Name the blood parasite species.
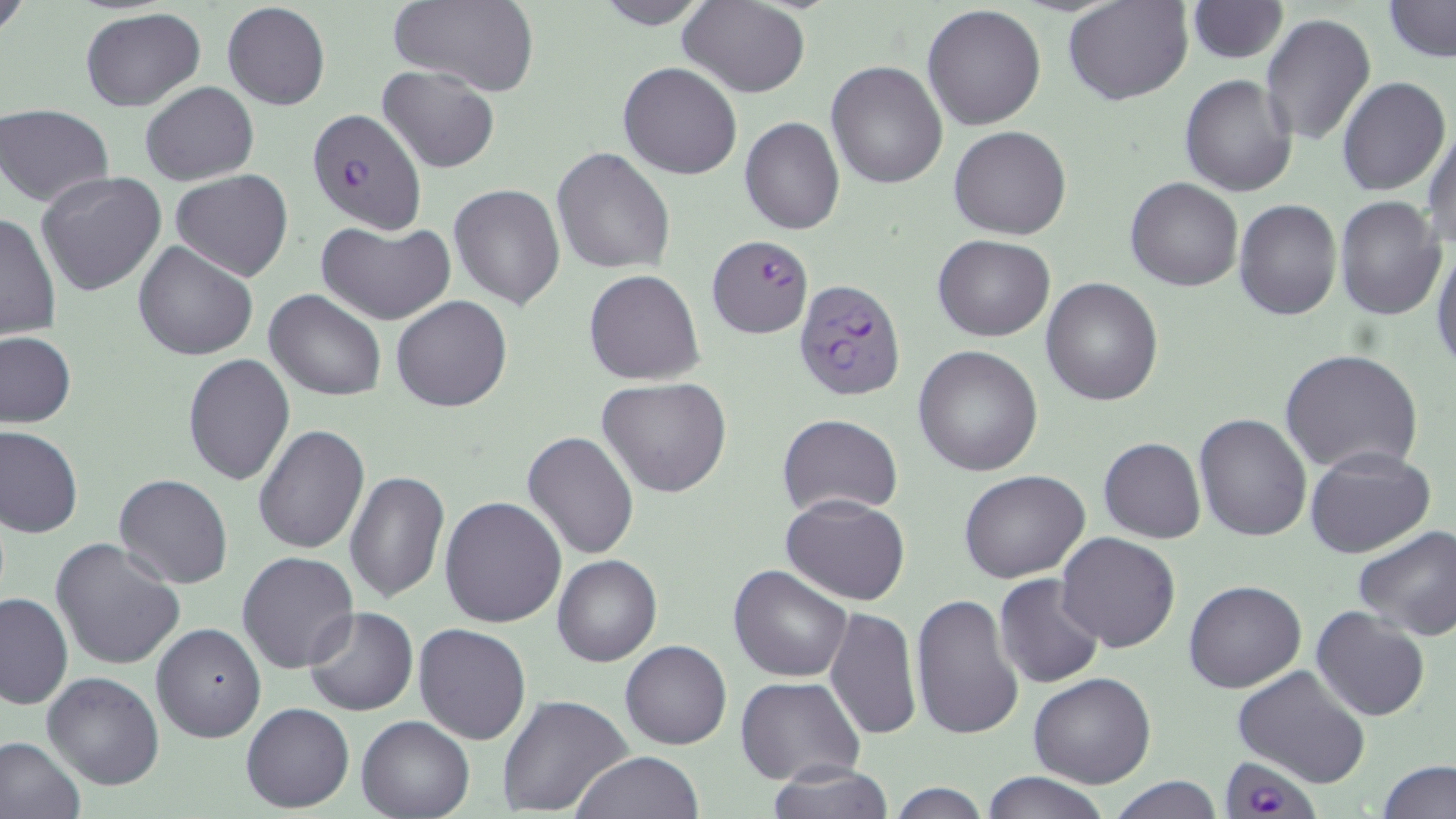
Plasmodium falciparum.

Approximate bounding boxes as [x1, y1, x2, y2] in pixels. Plasmodium falciparum-infected red blood cell locations (subset): [707, 234, 814, 338], [792, 279, 905, 400], [1220, 759, 1325, 818]. Uninfected red blood cell locations (subset): [0, 0, 30, 39], [385, 0, 539, 96], [593, 0, 716, 28], [1064, 0, 1193, 106], [1381, 0, 1455, 61], [681, 1, 810, 97], [1187, 1, 1288, 62], [222, 2, 330, 111], [922, 4, 1047, 131], [79, 7, 207, 111], [1261, 13, 1376, 145], [827, 60, 947, 189], [618, 62, 743, 180], [379, 64, 501, 174], [1179, 74, 1297, 197], [1336, 75, 1450, 195], [141, 80, 259, 186], [0, 104, 115, 207], [740, 116, 845, 235], [1423, 120, 1456, 255], [950, 125, 1071, 240], [551, 147, 675, 274], [169, 169, 293, 280], [36, 171, 168, 297], [1126, 177, 1244, 291], [449, 183, 565, 310], [1335, 196, 1446, 320], [1233, 200, 1341, 320], [0, 212, 61, 340], [317, 221, 456, 324], [934, 236, 1055, 340], [133, 241, 258, 362], [1430, 242, 1455, 370], [583, 269, 705, 386], [1041, 278, 1164, 406], [264, 289, 387, 400], [390, 295, 512, 412], [0, 330, 76, 427], [913, 345, 1043, 477], [1279, 349, 1424, 477], [183, 353, 296, 486], [597, 377, 733, 497], [777, 413, 903, 519], [1192, 413, 1312, 542], [253, 423, 371, 554], [1, 425, 83, 538], [522, 430, 638, 560], [1098, 436, 1206, 544], [1303, 448, 1436, 558], [343, 469, 450, 605], [959, 469, 1092, 583], [114, 474, 235, 589], [781, 493, 912, 605], [439, 495, 568, 628], [1353, 525, 1456, 642], [1056, 532, 1181, 653], [51, 537, 185, 671], [237, 552, 359, 674], [552, 553, 662, 667], [729, 564, 852, 682], [994, 574, 1107, 691], [1183, 579, 1307, 693], [0, 591, 74, 708], [911, 593, 1023, 740], [1310, 605, 1431, 722], [302, 606, 418, 715], [824, 606, 921, 741], [151, 622, 267, 742], [415, 622, 532, 745], [621, 641, 732, 750], [1232, 665, 1373, 787], [43, 672, 164, 789], [1028, 674, 1156, 788], [736, 677, 865, 787], [497, 693, 633, 817], [241, 703, 354, 812], [358, 715, 473, 819], [0, 736, 86, 819], [573, 751, 704, 818], [1378, 759, 1455, 818], [763, 765, 895, 818], [979, 771, 1108, 819], [1108, 777, 1225, 818], [884, 783, 995, 818]. One field of a larger specimen. Thin blood smear. 1000x magnification. Image is 1456×819 pixels. Light microscopy. May-Grünwald-Giemsa-stained preparation.